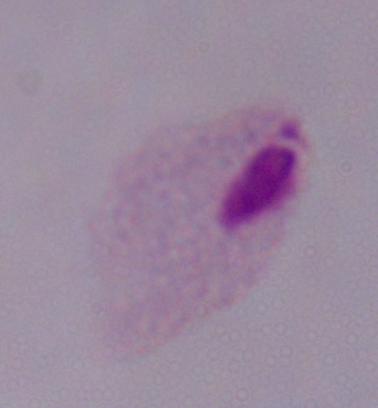
modality = micrograph
magnification = 1000x
identification = trichomonad